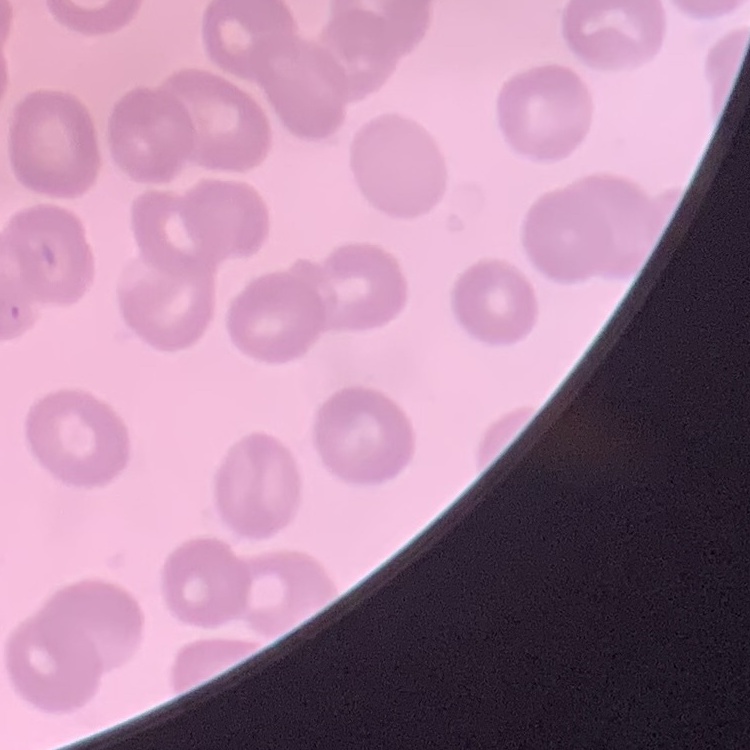

Summary:
  - Red blood cell morphology: no rouleaux formation
  - Image type: one tile cut from a larger photomicrograph
  - Preparation: thin peripheral smear
  - Stain: Field's or Giemsa